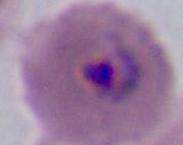
Summary:
  - Identification: Plasmodium
  - Modality: photomicrograph
  - Magnification: 400x or 1000x